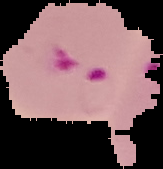
Cell region segmented out of the field of view; the surrounding area is masked to black. From a thin blood film. Image is 163×169 pixels. Malaria status: parasitized.